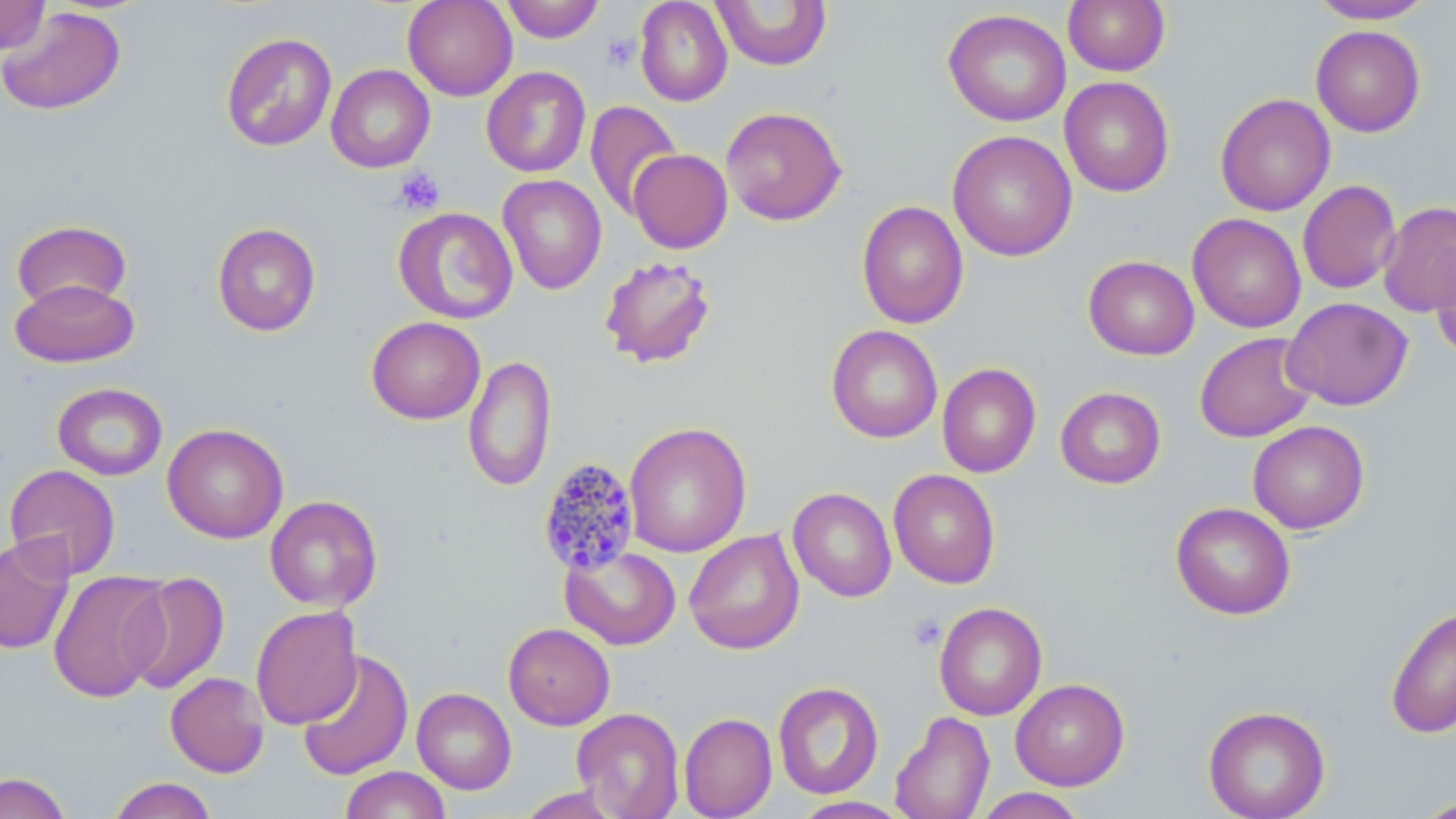

slide-level diagnosis = Plasmodium malariae
platelet locations = approximate bounding boxes as (x1,y1)-(x2,y2) corner pairs in pixels: (601,33)-(641,72), (392,167)-(446,216), (908,613)-(946,652)
Plasmodium malariae-infected red blood cell locations = approximate bounding boxes as (x1,y1)-(x2,y2) corner pairs in pixels: (537,457)-(642,575)
image size = 1456×819 pixels
modality = optical microscopy
preparation = thin blood film
field of view = one of a larger specimen
stain = May-Grünwald-Giemsa
uninfected red blood cell locations = approximate bounding boxes as (x1,y1)-(x2,y2) corner pairs in pixels: (0,0)-(51,55), (402,0)-(518,101), (500,0)-(605,43), (634,0)-(732,107), (1063,0)-(1170,76), (1309,0)-(1435,24), (711,1)-(832,71), (0,6)-(127,116), (943,8)-(1071,127), (1310,24)-(1426,137), (220,32)-(338,152), (326,64)-(435,173), (481,66)-(591,178), (1059,76)-(1175,197), (1215,93)-(1336,216), (585,100)-(682,220), (720,106)-(847,226), (947,130)-(1078,261), (628,149)-(732,253), (498,174)-(607,295), (1297,179)-(1401,295), (856,200)-(969,329), (1378,201)-(1456,316), (393,206)-(518,325), (1187,213)-(1306,333), (11,219)-(132,313), (212,222)-(321,337), (1429,239)-(1456,361), (599,255)-(717,369), (1083,255)-(1199,360), (10,278)-(139,368), (1282,297)-(1413,411), (366,316)-(486,424), (826,324)-(942,443), (1194,331)-(1319,443), (463,355)-(557,492), (937,362)-(1041,478), (52,382)-(167,481), (1055,386)-(1166,489), (1247,420)-(1369,534), (624,422)-(751,557), (162,423)-(289,543), (3,464)-(121,579), (888,469)-(1001,589), (787,487)-(897,602), (264,495)-(383,612), (1170,502)-(1296,620), (684,529)-(804,655), (0,535)-(75,655), (560,545)-(681,650), (47,570)-(171,702), (123,571)-(230,695), (934,602)-(1047,721), (1385,604)-(1456,739), (249,605)-(362,730), (503,623)-(615,730), (297,648)-(413,782), (165,672)-(270,778), (1010,678)-(1130,790), (773,681)-(884,799), (412,687)-(517,794), (1203,705)-(1331,819), (678,706)-(882,811), (571,707)-(685,819), (890,710)-(995,819), (679,712)-(777,819), (339,766)-(451,819), (0,772)-(71,819), (107,777)-(218,819), (517,787)-(623,818), (973,787)-(1089,818), (1410,795)-(1456,818), (791,796)-(912,819)
magnification = 1000x